Locate platelets.
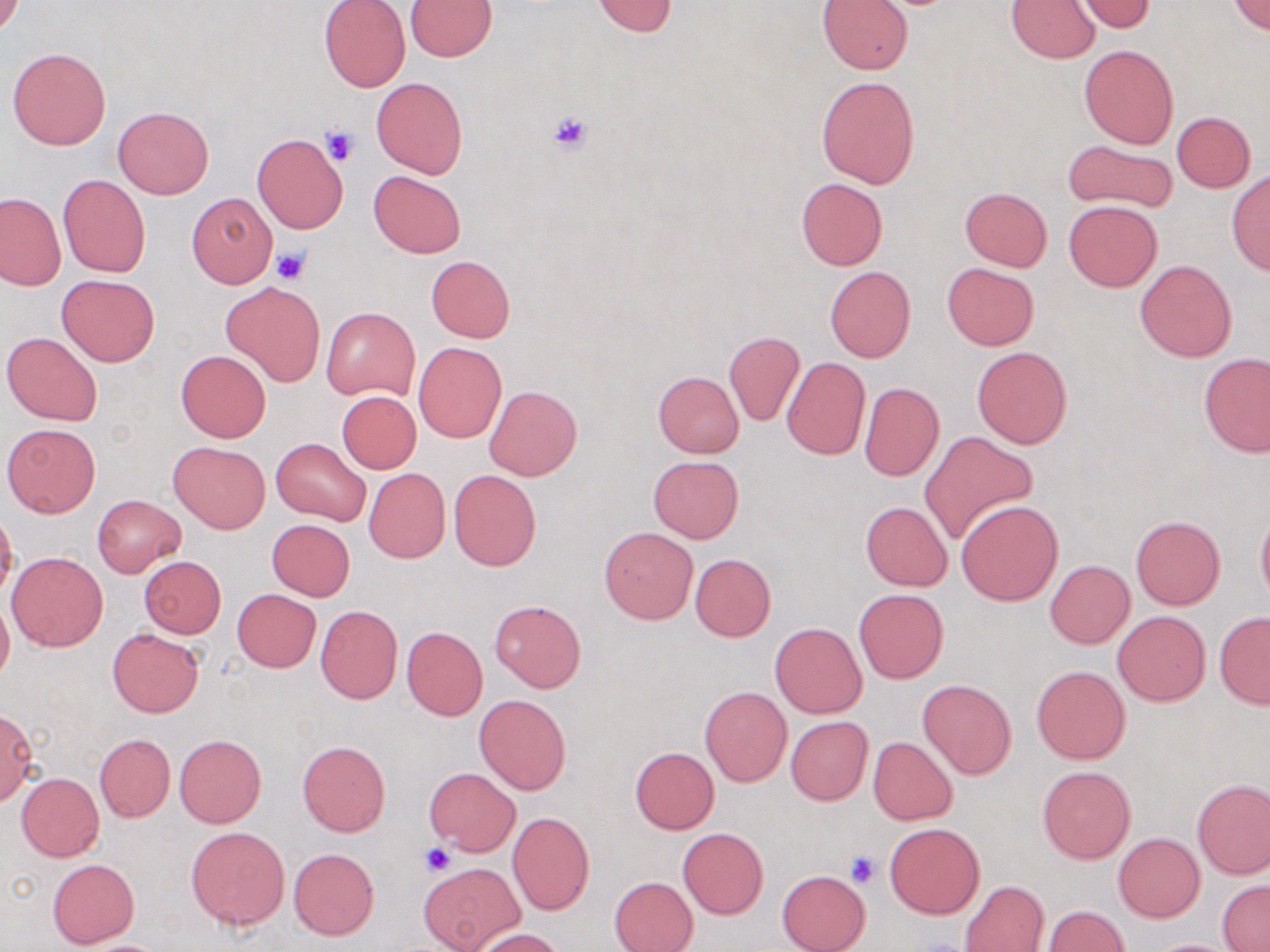
Approximate bounding boxes as named x1/y1/x2/y2 corners in pixels.
Platelets: (x1=545, y1=110, x2=595, y2=155), (x1=319, y1=127, x2=360, y2=166), (x1=271, y1=246, x2=310, y2=285), (x1=422, y1=842, x2=456, y2=877), (x1=845, y1=851, x2=880, y2=888).

{
  "slide_level_diagnosis": "negative for blood parasites",
  "image_size": "1270×952 pixels",
  "uninfected_red_blood_cell_locations": "approximate bounding boxes as named x1/y1/x2/y2 corners in pixels: (x1=319, y1=0, x2=411, y2=92), (x1=818, y1=0, x2=913, y2=74), (x1=1006, y1=0, x2=1099, y2=63), (x1=406, y1=1, x2=495, y2=60), (x1=590, y1=1, x2=679, y2=37), (x1=1072, y1=1, x2=1156, y2=33), (x1=1230, y1=2, x2=1270, y2=35), (x1=1079, y1=45, x2=1178, y2=147), (x1=8, y1=46, x2=112, y2=151), (x1=817, y1=75, x2=919, y2=187), (x1=371, y1=76, x2=468, y2=180), (x1=113, y1=107, x2=214, y2=199), (x1=1170, y1=110, x2=1255, y2=192), (x1=252, y1=133, x2=348, y2=233), (x1=1063, y1=138, x2=1176, y2=214), (x1=369, y1=171, x2=466, y2=258), (x1=1226, y1=171, x2=1270, y2=275), (x1=58, y1=175, x2=150, y2=277), (x1=796, y1=177, x2=887, y2=269), (x1=959, y1=187, x2=1052, y2=270), (x1=0, y1=193, x2=64, y2=290), (x1=187, y1=193, x2=277, y2=288), (x1=1063, y1=201, x2=1162, y2=292), (x1=426, y1=256, x2=515, y2=342), (x1=1135, y1=259, x2=1236, y2=361), (x1=941, y1=263, x2=1038, y2=350), (x1=824, y1=267, x2=915, y2=362), (x1=58, y1=274, x2=158, y2=366), (x1=222, y1=282, x2=325, y2=386), (x1=322, y1=306, x2=419, y2=402), (x1=724, y1=331, x2=805, y2=426), (x1=2, y1=332, x2=102, y2=425), (x1=414, y1=342, x2=506, y2=442), (x1=972, y1=347, x2=1072, y2=448), (x1=177, y1=350, x2=270, y2=442), (x1=1199, y1=352, x2=1269, y2=457), (x1=781, y1=356, x2=870, y2=460), (x1=654, y1=372, x2=743, y2=455), (x1=859, y1=382, x2=945, y2=481), (x1=485, y1=385, x2=582, y2=480), (x1=337, y1=391, x2=421, y2=473), (x1=877, y1=393, x2=983, y2=502), (x1=3, y1=424, x2=100, y2=518), (x1=919, y1=431, x2=1039, y2=547), (x1=271, y1=437, x2=372, y2=527), (x1=168, y1=441, x2=270, y2=533), (x1=648, y1=456, x2=742, y2=543), (x1=364, y1=468, x2=450, y2=563), (x1=448, y1=469, x2=541, y2=571), (x1=92, y1=495, x2=184, y2=577), (x1=956, y1=500, x2=1064, y2=605), (x1=860, y1=501, x2=952, y2=590), (x1=1256, y1=503, x2=1270, y2=606), (x1=0, y1=509, x2=18, y2=602), (x1=1131, y1=516, x2=1225, y2=610), (x1=266, y1=519, x2=354, y2=601), (x1=601, y1=527, x2=697, y2=623), (x1=7, y1=552, x2=108, y2=651), (x1=690, y1=554, x2=776, y2=641), (x1=139, y1=556, x2=225, y2=638), (x1=1045, y1=560, x2=1134, y2=648), (x1=855, y1=588, x2=948, y2=682), (x1=231, y1=589, x2=321, y2=672), (x1=0, y1=596, x2=13, y2=686), (x1=489, y1=599, x2=586, y2=691), (x1=314, y1=606, x2=402, y2=703), (x1=1113, y1=610, x2=1210, y2=706), (x1=1214, y1=612, x2=1270, y2=709), (x1=770, y1=622, x2=866, y2=718), (x1=401, y1=626, x2=488, y2=720), (x1=107, y1=628, x2=204, y2=717), (x1=1031, y1=665, x2=1130, y2=764), (x1=918, y1=679, x2=1015, y2=778), (x1=699, y1=685, x2=793, y2=786), (x1=474, y1=694, x2=571, y2=795), (x1=0, y1=706, x2=38, y2=805), (x1=786, y1=716, x2=873, y2=804), (x1=94, y1=733, x2=175, y2=823), (x1=175, y1=735, x2=266, y2=828), (x1=868, y1=736, x2=957, y2=825), (x1=296, y1=741, x2=392, y2=837), (x1=629, y1=746, x2=719, y2=833), (x1=1037, y1=766, x2=1134, y2=863), (x1=425, y1=768, x2=520, y2=856), (x1=16, y1=772, x2=104, y2=861), (x1=1192, y1=779, x2=1270, y2=879), (x1=507, y1=811, x2=594, y2=914), (x1=885, y1=823, x2=984, y2=918), (x1=186, y1=826, x2=289, y2=930), (x1=677, y1=827, x2=769, y2=919), (x1=1113, y1=832, x2=1204, y2=922), (x1=288, y1=847, x2=379, y2=939), (x1=47, y1=859, x2=140, y2=947), (x1=419, y1=861, x2=523, y2=951), (x1=776, y1=869, x2=870, y2=952), (x1=609, y1=876, x2=698, y2=952), (x1=960, y1=879, x2=1049, y2=952), (x1=1218, y1=882, x2=1270, y2=951), (x1=1042, y1=905, x2=1128, y2=952), (x1=471, y1=928, x2=564, y2=951), (x1=73, y1=939, x2=173, y2=952), (x1=1146, y1=939, x2=1239, y2=952)",
  "magnification": "1000x",
  "stain": "May-Grünwald-Giemsa",
  "field_of_view": "one of a larger specimen",
  "preparation": "thin blood film",
  "modality": "light microscopy"
}